Report the malaria status of this cell.
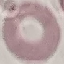

It is uninfected.

image type = automatically extracted cell patch, resized to 64 × 64 pixels
capture = smartphone through the microscope eyepiece
stain = Giemsa
preparation = thin blood film